Locate every malaria parasite.
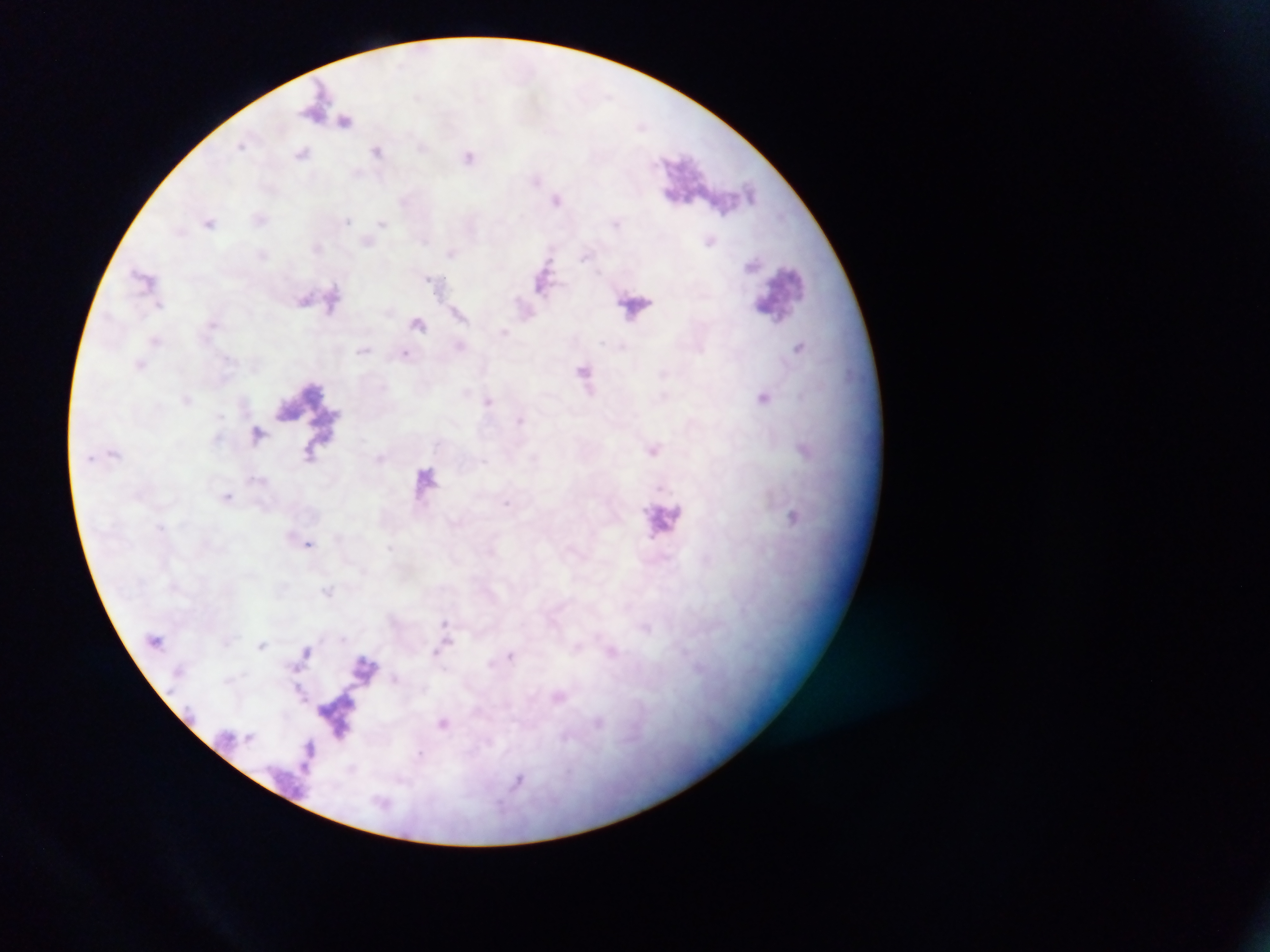
Approximate centers as (x, y) in pixels.
Malaria parasites: (240, 145), (378, 150), (302, 153), (469, 157), (348, 221), (209, 222), (143, 276), (159, 304), (405, 353), (506, 504), (309, 543), (445, 622), (511, 656).

field_of_view: single
preparation: thick blood film
capture: mobile-phone photograph through a microscope
country: Ghana
image_size: 1270×952 pixels